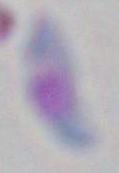

identification = Toxoplasma gondii
modality = micrograph
magnification = 1000x